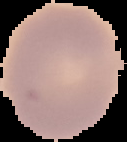
Summary:
  - Image size: 127×142 pixels
  - Image type: segmented cell region with the area outside set to black
  - Preparation: thin blood smear
  - Result: negative for malaria parasites